State which parasite is depicted.
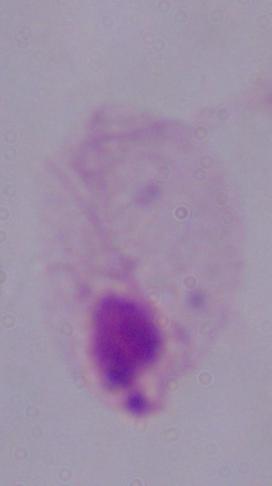

A trichomonad.

Summary:
  - Magnification: 1000x
  - Modality: photomicrograph